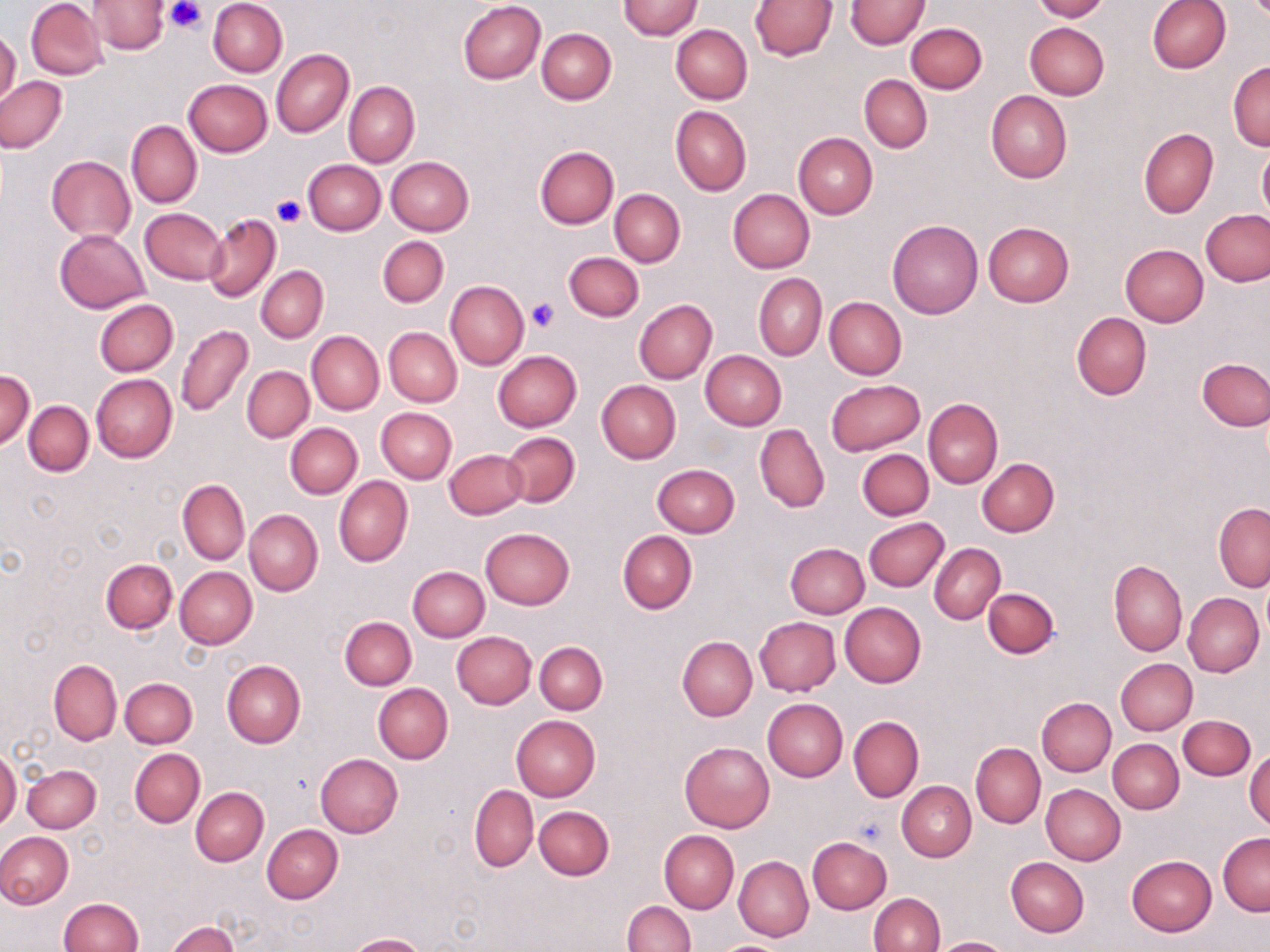

Approximate bounding boxes as (x1,y1)-(x2,y2) corner pairs in pixels. Uninfected red blood cell locations: (26,0)-(108,80), (87,0)-(168,55), (208,0)-(288,77), (619,0)-(702,40), (750,0)-(838,60), (846,0)-(929,48), (1031,0)-(1109,22), (458,1)-(547,84), (1146,1)-(1230,74), (906,22)-(987,94), (1025,22)-(1109,99), (672,24)-(752,103), (537,29)-(616,104), (0,30)-(21,108), (272,50)-(353,137), (1228,61)-(1270,151), (860,75)-(932,153), (1,76)-(67,153), (183,79)-(272,156), (343,81)-(419,167), (986,91)-(1071,183), (670,106)-(750,196), (126,120)-(202,208), (1138,128)-(1219,217), (793,132)-(877,219), (533,145)-(618,228), (1257,146)-(1270,223), (47,155)-(136,244), (386,156)-(474,235), (303,160)-(386,235), (609,189)-(685,267), (727,189)-(815,272), (140,207)-(229,284), (1200,209)-(1270,286), (203,212)-(281,302), (887,219)-(983,319), (983,222)-(1074,307), (55,229)-(149,312), (377,236)-(448,308), (1120,244)-(1208,326), (562,251)-(644,323), (257,267)-(327,343), (753,273)-(826,361), (445,281)-(529,369), (824,297)-(906,379), (94,299)-(178,376), (633,299)-(717,384), (1072,312)-(1152,400), (176,324)-(253,416), (384,328)-(462,407), (307,331)-(384,415), (492,351)-(581,432), (700,351)-(786,430), (1198,357)-(1270,430), (242,366)-(314,442), (0,370)-(34,448), (91,372)-(177,463), (826,379)-(925,456), (596,380)-(681,463), (924,399)-(1002,488), (24,401)-(94,475), (377,407)-(456,484), (285,422)-(362,499), (754,424)-(829,513), (501,431)-(581,509), (444,448)-(528,519), (857,448)-(934,520), (977,458)-(1059,536), (652,464)-(740,538), (334,475)-(413,568), (178,479)-(250,565), (1215,503)-(1270,592), (244,509)-(322,595), (863,517)-(950,592), (481,527)-(574,609), (617,530)-(697,615), (785,543)-(870,618), (929,543)-(1005,625), (101,559)-(178,634), (1109,559)-(1187,656), (175,566)-(257,649), (407,566)-(489,642), (983,587)-(1059,659), (1183,592)-(1265,677), (839,603)-(926,687), (754,617)-(840,696), (339,618)-(415,690), (452,631)-(536,708), (677,636)-(758,721), (535,642)-(607,714), (1116,658)-(1197,734), (222,659)-(306,747), (49,660)-(122,746), (120,677)-(196,748), (373,684)-(452,763), (1037,697)-(1116,776), (762,699)-(848,782), (511,715)-(601,801), (1179,715)-(1254,780), (848,716)-(923,802), (1108,739)-(1184,813), (679,742)-(775,832), (971,743)-(1045,828), (130,748)-(205,827), (0,749)-(20,831), (1245,749)-(1270,830), (314,753)-(403,837), (23,764)-(101,833), (897,781)-(976,861), (1040,784)-(1125,865), (469,785)-(538,872), (191,787)-(268,866), (535,806)-(614,880), (261,824)-(342,904), (0,831)-(74,908), (659,831)-(739,912), (1218,833)-(1270,915), (807,837)-(892,914), (733,849)-(886,926), (1126,855)-(1217,936), (733,856)-(813,942), (1006,857)-(1089,937), (869,893)-(945,952), (58,898)-(143,951), (623,901)-(695,952), (166,921)-(239,952), (345,933)-(427,952), (929,937)-(1016,952). Platelet locations: (166,0)-(205,33), (272,195)-(304,225), (527,297)-(558,331). Slide-level diagnosis: no evidence of blood parasites. Optical microscopy. Thin blood film. One field of a larger specimen. Image is 1270×952 pixels. 1000x magnification. May-Grünwald-Giemsa stain.